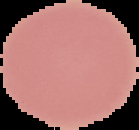
image_type: cell region segmented out of the field of view; surrounding area masked to black
preparation: thin blood smear
result: no malaria parasites seen
image_size: 139×130 pixels